Comment on the morphology of the red blood cells.
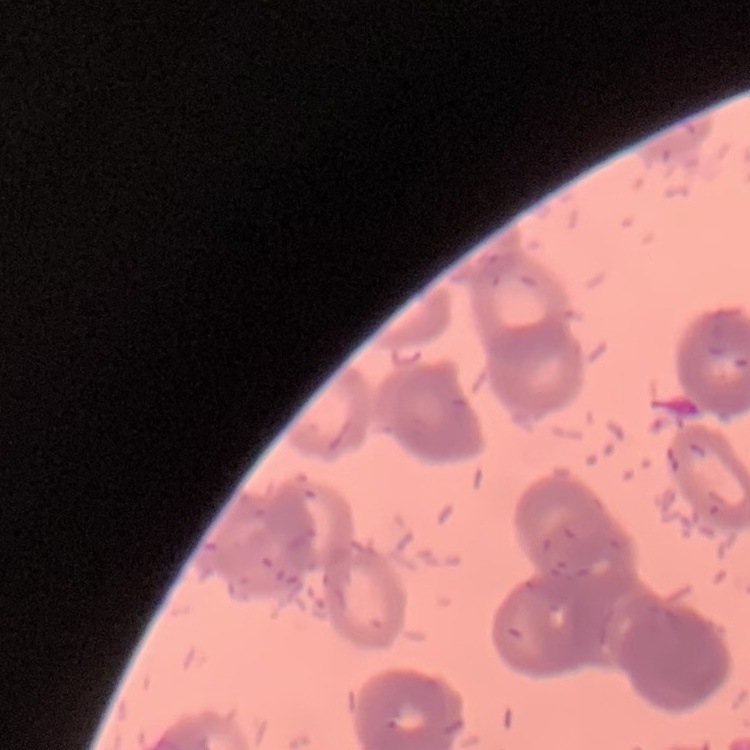
Rouleaux formation.

Square crop of a larger photomicrograph. Thin blood film. Stained with either Field's or Giemsa.